Give the position of every Plasmodium parasite and every leukocyte.
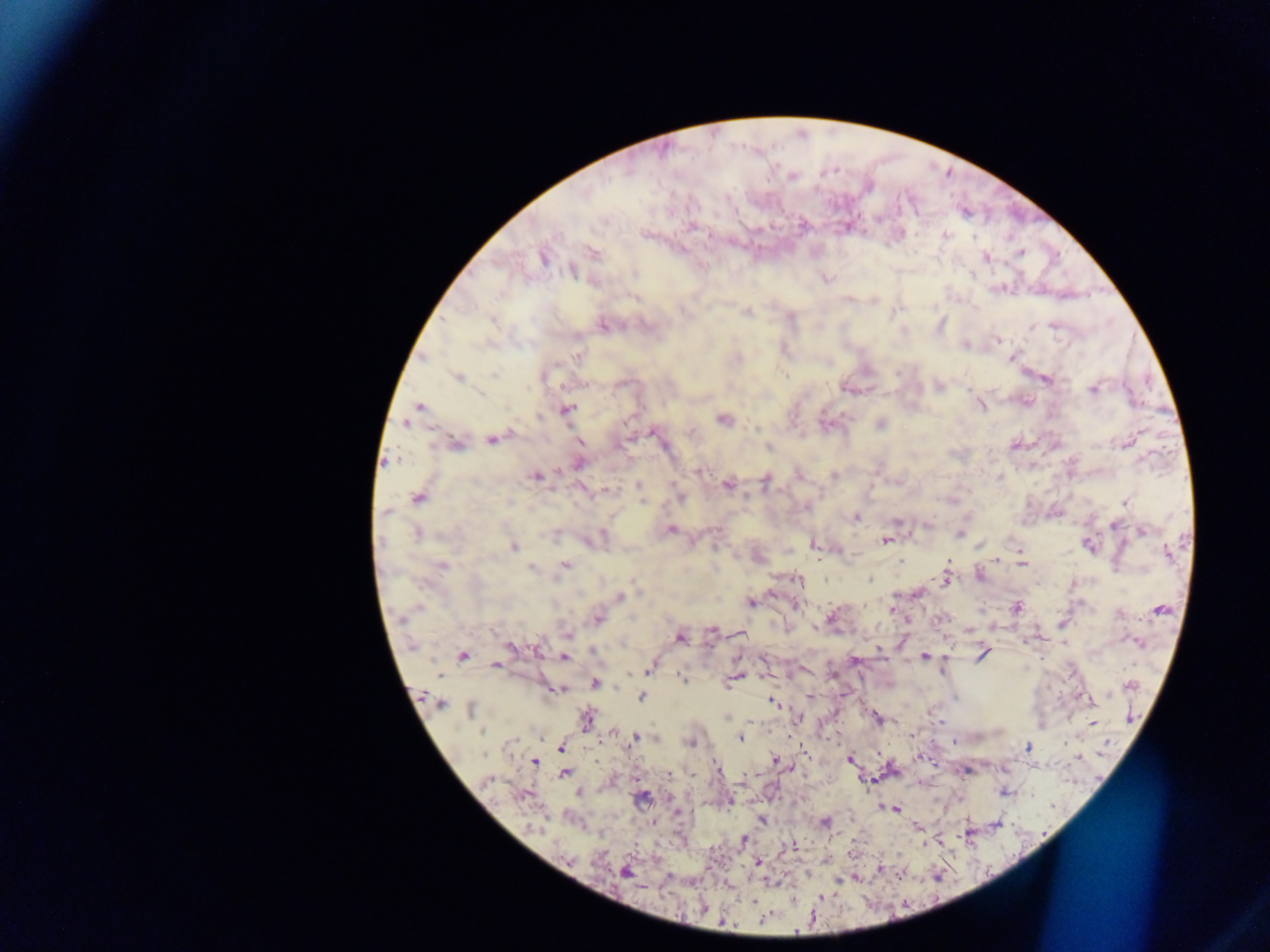

Approximate centers as {x, y} in pixels.
Plasmodium parasites: {793, 176}, {802, 226}, {847, 227}, {943, 235}, {592, 252}, {1020, 253}, {985, 257}, {542, 258}, {572, 271}, {825, 279}, {873, 299}, {747, 311}, {604, 325}, {939, 325}, {996, 340}, {964, 344}, {577, 355}, {1012, 357}, {458, 377}, {1045, 378}, {938, 386}, {1093, 389}, {980, 405}, {419, 407}, {565, 410}, {722, 418}, {407, 421}, {880, 424}, {652, 431}, {492, 438}, {455, 443}, {579, 443}, {1014, 445}, {768, 446}, {578, 462}, {700, 470}, {536, 476}, {834, 476}, {765, 480}, {727, 485}, {639, 487}, {607, 490}, {679, 496}, {418, 497}, {1125, 502}, {855, 517}, {1113, 524}, {927, 525}, {670, 530}, {1142, 530}, {416, 533}, {958, 533}, {596, 539}, {885, 540}, {814, 543}, {1088, 544}, {513, 547}, {1018, 550}, {1166, 552}, {757, 556}, {996, 558}, {1019, 558}, {441, 565}, {564, 565}, {1020, 565}, {532, 567}, {979, 575}, {945, 577}, {797, 579}, {918, 592}, {619, 597}, {750, 602}, {795, 605}, {1016, 607}, {892, 609}, {1159, 609}, {832, 617}, {597, 618}, {906, 620}, {713, 630}, {969, 630}, {740, 632}, {568, 633}, {679, 637}, {1138, 641}, {511, 646}, {878, 648}, {982, 653}, {462, 655}, {924, 656}, {564, 657}, {853, 660}, {496, 665}, {649, 667}, {681, 676}, {734, 678}, {594, 683}, {1131, 685}, {556, 688}, {810, 696}, {640, 697}, {1090, 699}, {772, 702}, {439, 703}, {471, 709}, {797, 718}, {877, 718}, {586, 719}, {940, 722}, {1091, 723}, {613, 733}, {911, 734}, {635, 737}, {740, 737}, {689, 741}, {560, 746}, {1027, 748}, {919, 757}, {1078, 757}, {774, 759}, {850, 759}, {534, 760}, {716, 765}, {564, 774}, {667, 774}, {1004, 791}, {578, 793}, {524, 795}, {641, 797}, {729, 800}, {894, 809}, {677, 813}, {762, 820}, {824, 822}, {996, 823}, {917, 827}, {743, 840}, {938, 840}, {793, 847}, {757, 862}, {880, 868}, {623, 871}, {854, 877}, {839, 879}, {727, 885}.
No leukocytes observed.

Summary:
  - Field of view: single
  - Country: Ghana
  - Preparation: thick blood smear
  - Capture: mobile-phone photograph through a microscope
  - Image size: 1270×952 pixels